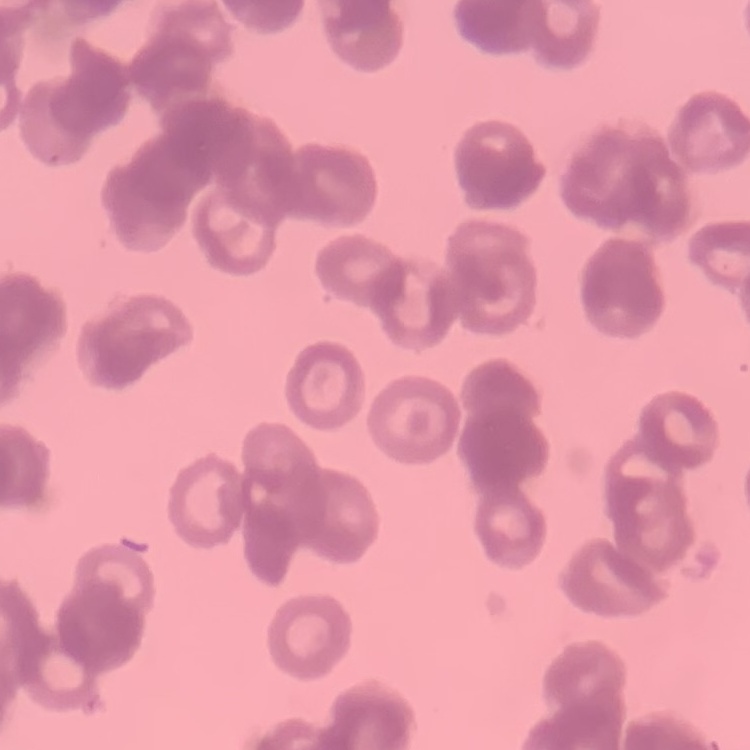 The red blood cells show rouleaux formation. Square crop of a larger photomicrograph. Thin blood smear. Stained with either Field's or Giemsa.